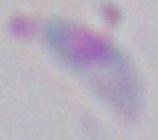 Toxoplasma gondii is shown. Captured at 1000x magnification. Micrograph.